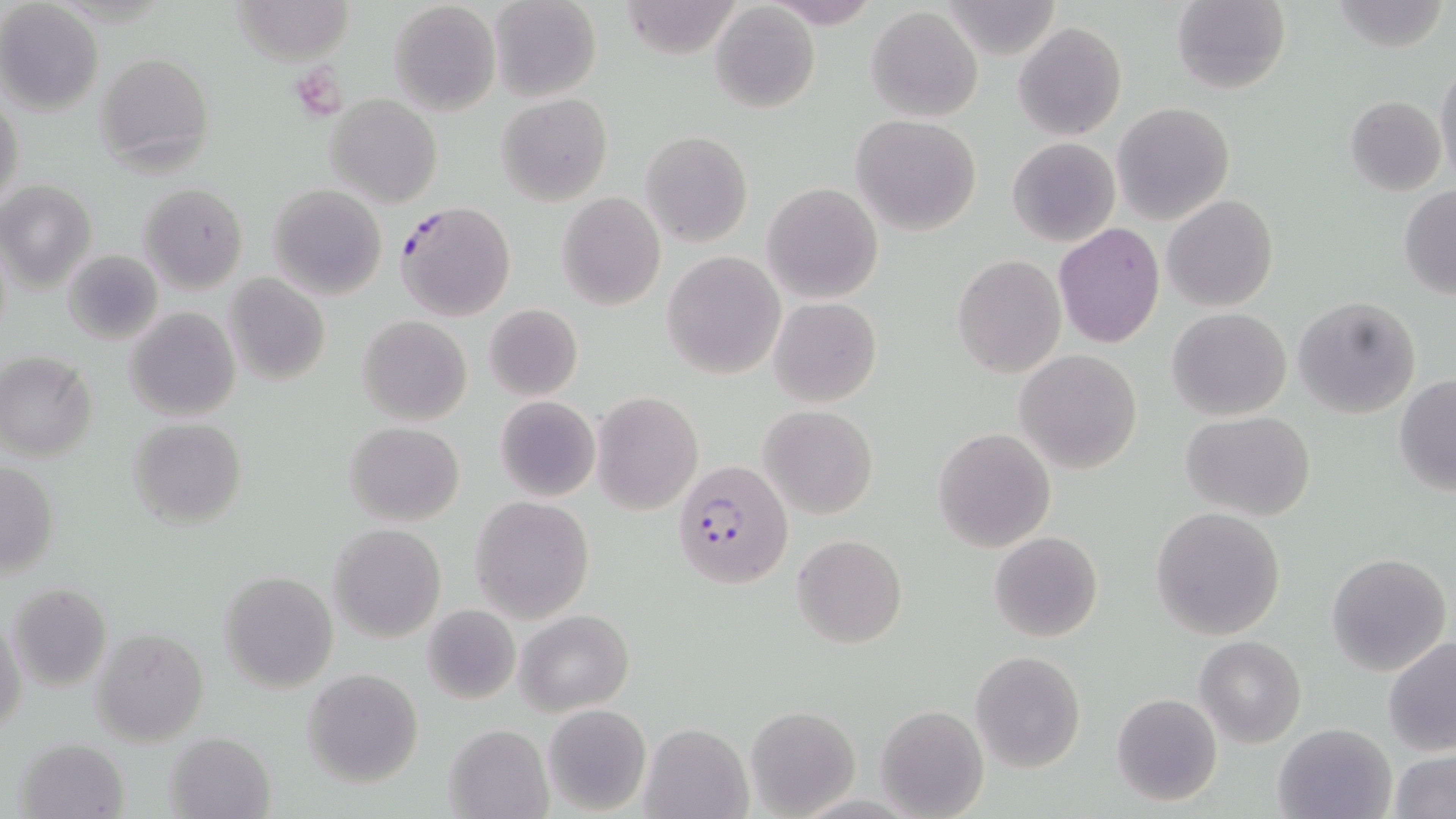

slide-level diagnosis = Plasmodium falciparum
magnification = 1000x
platelet locations = approximate bounding boxes as (x1, y1, x2, y2) in pixels: (292, 65, 348, 120)
stain = May-Grünwald-Giemsa
field of view = one of a larger specimen
preparation = thin blood film
modality = optical microscopy
Plasmodium falciparum-infected red blood cell locations = approximate bounding boxes as (x1, y1, x2, y2) in pixels: (396, 201, 517, 321), (672, 459, 794, 590)
uninfected red blood cell locations = approximate bounding boxes as (x1, y1, x2, y2) in pixels: (233, 0, 354, 65), (489, 0, 601, 103), (764, 0, 881, 29), (944, 0, 1062, 60), (1172, 0, 1291, 96), (1332, 0, 1450, 52), (388, 1, 500, 118), (618, 2, 746, 59), (0, 3, 104, 115), (708, 4, 821, 114), (867, 7, 983, 122), (1014, 22, 1126, 140), (94, 51, 216, 174), (1433, 57, 1456, 184), (497, 93, 612, 205), (1, 94, 25, 210), (326, 94, 442, 207), (1345, 95, 1446, 195), (1112, 102, 1234, 224), (851, 115, 982, 237), (641, 130, 753, 246), (1007, 137, 1120, 247), (1, 179, 96, 293), (139, 182, 248, 292), (761, 182, 883, 304), (267, 185, 388, 300), (1399, 185, 1456, 299), (556, 193, 666, 310), (1163, 195, 1280, 312), (1052, 223, 1166, 350), (62, 249, 161, 342), (661, 252, 785, 378), (953, 255, 1065, 378), (224, 273, 331, 386), (1292, 295, 1422, 420), (769, 297, 881, 407), (483, 303, 582, 402), (126, 307, 240, 422), (1167, 307, 1292, 420), (357, 316, 471, 425), (1015, 349, 1143, 473), (0, 352, 98, 462), (1394, 374, 1456, 497), (592, 391, 703, 514), (495, 395, 600, 503), (760, 405, 878, 519), (1180, 411, 1317, 522), (129, 417, 247, 528), (344, 421, 464, 527), (933, 428, 1056, 551), (1, 461, 60, 579), (470, 495, 595, 622), (1150, 508, 1285, 639), (328, 523, 446, 641), (988, 531, 1103, 642), (791, 535, 907, 649), (1326, 553, 1451, 675), (218, 571, 338, 692), (8, 582, 111, 693), (420, 602, 521, 706), (516, 609, 634, 715), (1, 610, 27, 743), (89, 626, 211, 748), (1195, 636, 1307, 748), (1382, 636, 1455, 756), (970, 652, 1085, 772), (303, 668, 424, 788), (1111, 692, 1223, 807), (542, 703, 651, 815), (745, 704, 861, 818), (876, 706, 987, 818), (640, 722, 753, 818), (1272, 722, 1396, 819), (443, 723, 553, 819), (165, 731, 277, 819), (13, 737, 130, 819), (1387, 749, 1455, 819)
image size = 1456×819 pixels